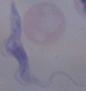
Summary:
  - Identification: trypanosome
  - Magnification: 1000x
  - Modality: micrograph